Identify the blood parasite species.
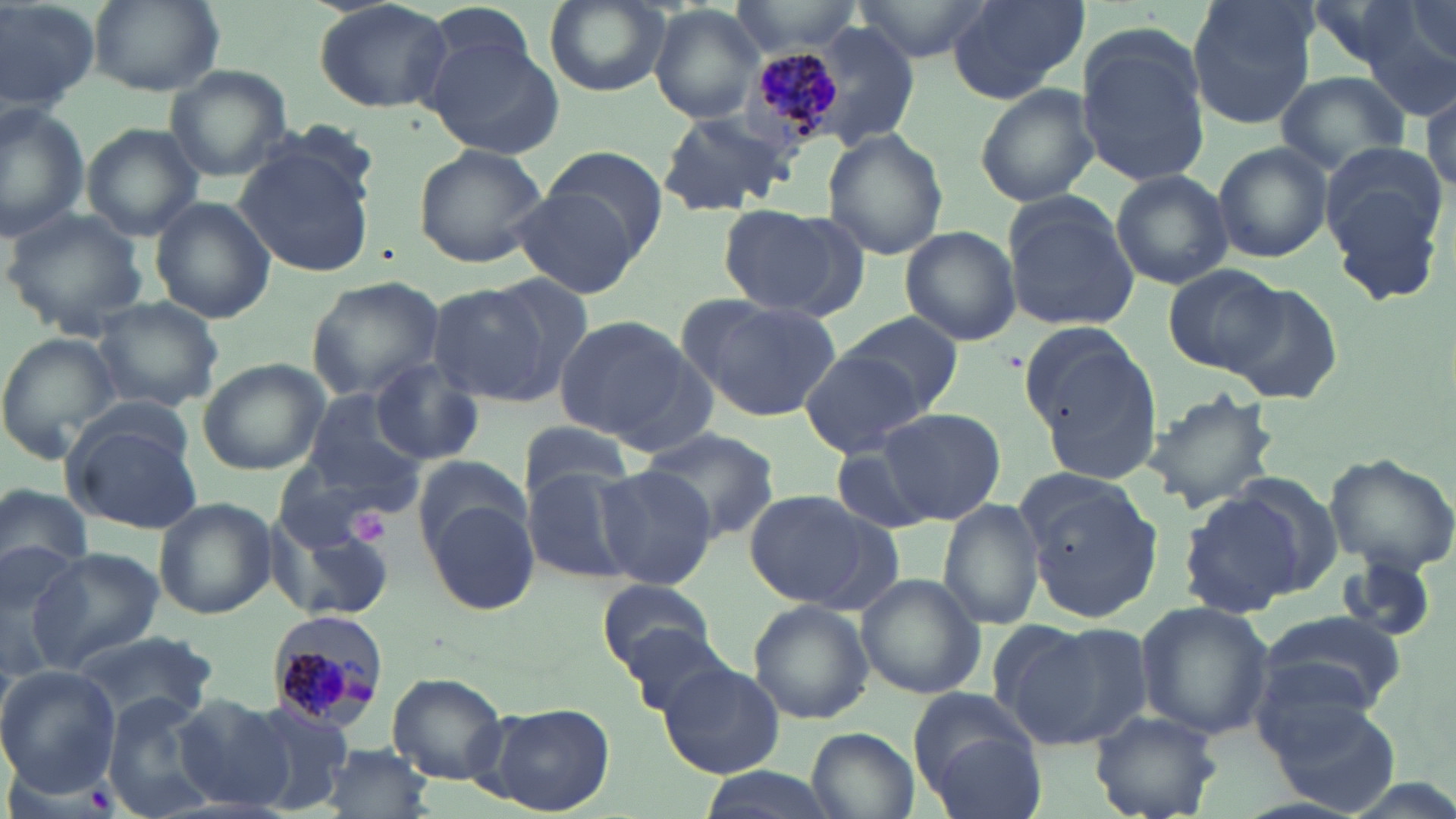

Plasmodium malariae.

Approximate bounding boxes as (x1, y1, x2, y2) in pixels. Uninfected red blood cell locations: (0, 0, 99, 116), (87, 0, 223, 96), (311, 0, 455, 114), (722, 0, 870, 56), (860, 0, 999, 62), (946, 0, 1089, 105), (1186, 0, 1319, 131), (1306, 0, 1431, 77), (1398, 0, 1454, 66), (543, 1, 669, 96), (1361, 1, 1455, 113), (650, 3, 765, 123), (800, 22, 919, 149), (1075, 26, 1212, 189), (426, 34, 567, 156), (162, 65, 294, 181), (1275, 70, 1411, 177), (1420, 77, 1456, 198), (974, 83, 1100, 209), (0, 101, 91, 240), (654, 109, 793, 217), (81, 123, 203, 241), (823, 129, 948, 261), (1211, 142, 1333, 263), (1317, 142, 1453, 309), (538, 143, 671, 261), (234, 144, 378, 279), (412, 144, 551, 268), (1110, 169, 1233, 289), (510, 184, 641, 299), (1001, 194, 1139, 331), (149, 197, 275, 323), (716, 203, 860, 319), (2, 208, 150, 337), (899, 226, 1021, 348), (1163, 263, 1284, 374), (304, 275, 447, 401), (425, 278, 572, 409), (1228, 282, 1342, 404), (683, 297, 842, 424), (90, 299, 227, 411), (839, 312, 964, 419), (552, 315, 697, 444), (1018, 323, 1145, 435), (0, 334, 121, 464), (1034, 345, 1164, 483), (799, 348, 933, 458), (197, 357, 331, 475), (368, 359, 484, 466), (298, 388, 430, 501), (1139, 389, 1275, 515), (874, 405, 1007, 525), (64, 417, 205, 534), (513, 421, 637, 503), (637, 429, 780, 541), (827, 442, 945, 538), (1322, 452, 1456, 575), (412, 455, 532, 559), (273, 458, 402, 552), (592, 464, 718, 588), (521, 467, 641, 585), (1017, 477, 1166, 623), (0, 481, 95, 586), (744, 488, 893, 610), (1180, 493, 1312, 618), (424, 497, 539, 616), (153, 498, 275, 618), (940, 499, 1044, 632), (277, 513, 396, 623), (0, 542, 98, 681), (28, 548, 162, 672), (856, 574, 985, 699), (597, 578, 715, 676), (747, 600, 875, 725), (1135, 600, 1276, 741), (1256, 611, 1407, 717), (991, 618, 1149, 748), (614, 619, 740, 723), (69, 630, 219, 725), (658, 661, 783, 778), (0, 666, 120, 797), (387, 672, 508, 786), (909, 691, 1041, 808), (101, 694, 224, 819), (171, 694, 294, 813), (1267, 696, 1404, 817), (238, 698, 363, 815), (489, 702, 613, 816), (1091, 710, 1222, 818), (806, 728, 919, 819), (318, 742, 435, 818). Platelet locations: (347, 508, 389, 545). Plasmodium malariae-infected red blood cell locations: (741, 38, 848, 153), (264, 611, 392, 730). Single field of view. 1000x magnification. Image is 1456×819 pixels. May-Grünwald-Giemsa stain. Thin blood film. Optical microscopy.